Classify this cell by malaria status.
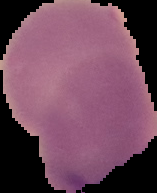
It is uninfected.

image type = segmented cell region with the area outside set to black
image size = 157×193 pixels
preparation = thin blood smear